Identify the blood parasite species.
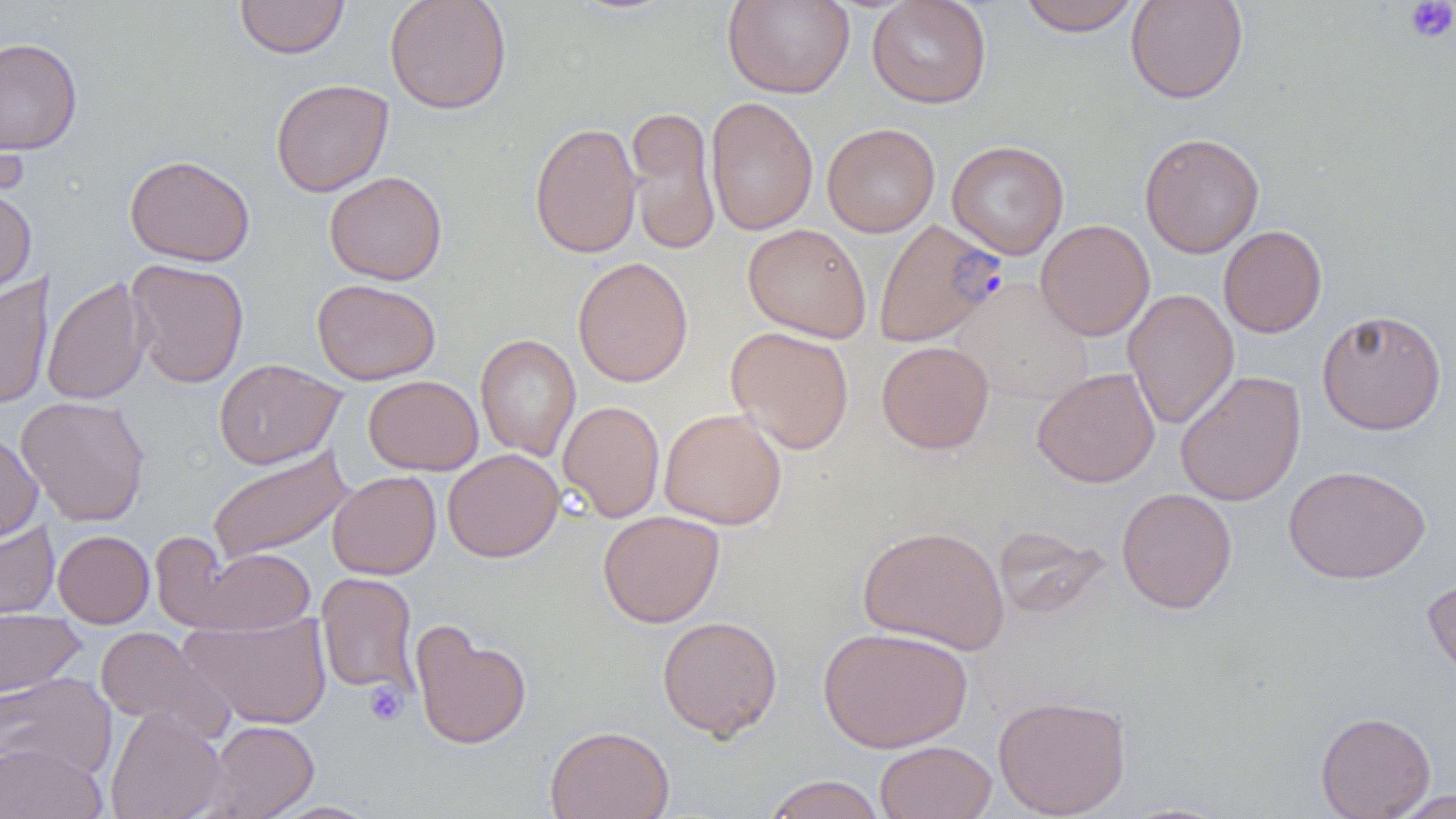

Plasmodium falciparum.

modality = optical microscopy
Plasmodium falciparum-infected red blood cell locations = approximate bounding boxes as (x1,y1)-(x2,y2) corner pairs in pixels: (873,218)-(1005,347)
preparation = thin blood film
magnification = 1000x
uninfected red blood cell locations = approximate bounding boxes as (x1,y1)-(x2,y2) corner pairs in pixels: (234,0)-(350,59), (384,0)-(512,115), (722,0)-(855,99), (867,0)-(991,108), (1017,0)-(1143,36), (1125,0)-(1249,104), (0,37)-(83,155), (270,78)-(394,197), (705,96)-(818,236), (625,105)-(721,256), (529,121)-(642,259), (822,123)-(940,237), (1140,132)-(1264,258), (947,140)-(1069,259), (124,154)-(255,266), (324,170)-(447,285), (0,187)-(37,297), (1035,219)-(1154,341), (743,223)-(871,342), (1219,225)-(1327,337), (572,257)-(693,387), (126,258)-(250,388), (0,274)-(54,410), (41,275)-(152,406), (312,279)-(441,385), (951,280)-(1095,405), (1122,289)-(1239,430), (1316,308)-(1447,435), (726,326)-(854,455), (475,334)-(581,462), (877,340)-(994,454), (213,358)-(346,469), (1032,367)-(1160,487), (1175,370)-(1306,507), (363,375)-(483,475), (15,395)-(151,526), (558,400)-(665,522), (659,408)-(787,530), (0,430)-(43,544), (207,445)-(353,565), (443,449)-(564,562), (1283,464)-(1431,584), (327,470)-(441,580), (1117,487)-(1238,614), (597,510)-(725,628), (0,520)-(60,626), (858,524)-(1010,654), (992,526)-(1110,620), (53,530)-(154,628), (181,544)-(315,636), (316,572)-(419,697), (1421,573)-(1456,688), (0,608)-(84,697), (179,612)-(332,729), (657,615)-(783,740), (410,622)-(532,750), (95,626)-(235,743), (818,626)-(973,752), (0,672)-(117,783), (992,693)-(1131,818), (105,707)-(227,819), (1315,710)-(1436,819), (203,720)-(319,819), (545,725)-(674,819), (874,740)-(997,819), (0,742)-(106,819), (762,774)-(886,819), (1386,789)-(1456,818), (263,801)-(382,818), (1111,801)-(1239,819)
image size = 1456×819 pixels
field of view = single
platelet locations = approximate bounding boxes as (x1,y1)-(x2,y2) corner pairs in pixels: (1405,1)-(1456,43), (363,680)-(408,726)